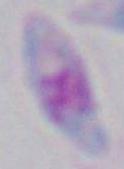
magnification = 1000x
identification = Toxoplasma gondii
modality = micrograph